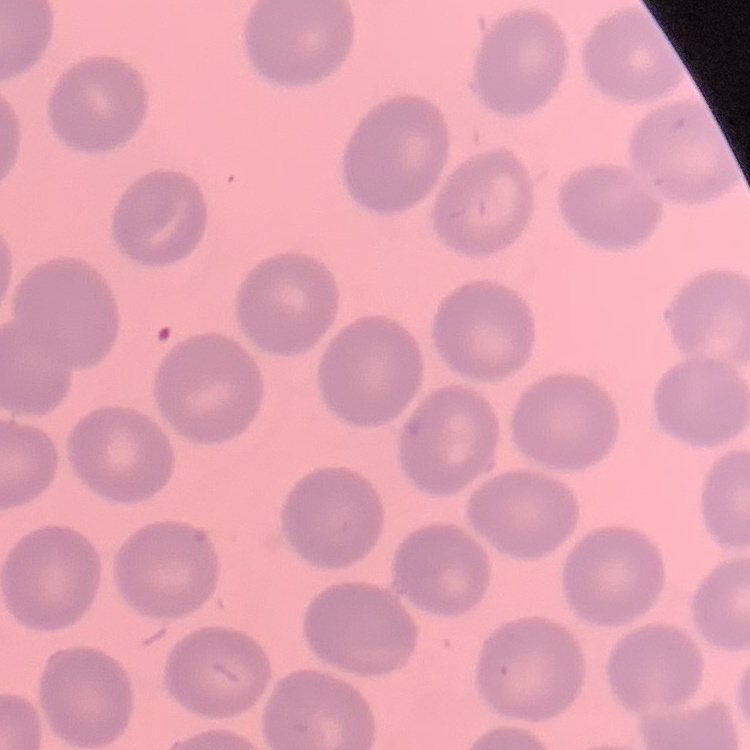 The erythrocytes show no rouleaux formation. Thin blood smear. Stained with either Field's or Giemsa. One tile cut from a larger photomicrograph.